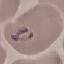

Malaria status: parasitized. Acquired by smartphone through the microscope eyepiece. Giemsa stain. Thin blood smear. Automatically extracted cell patch, resized to 64 × 64 pixels.